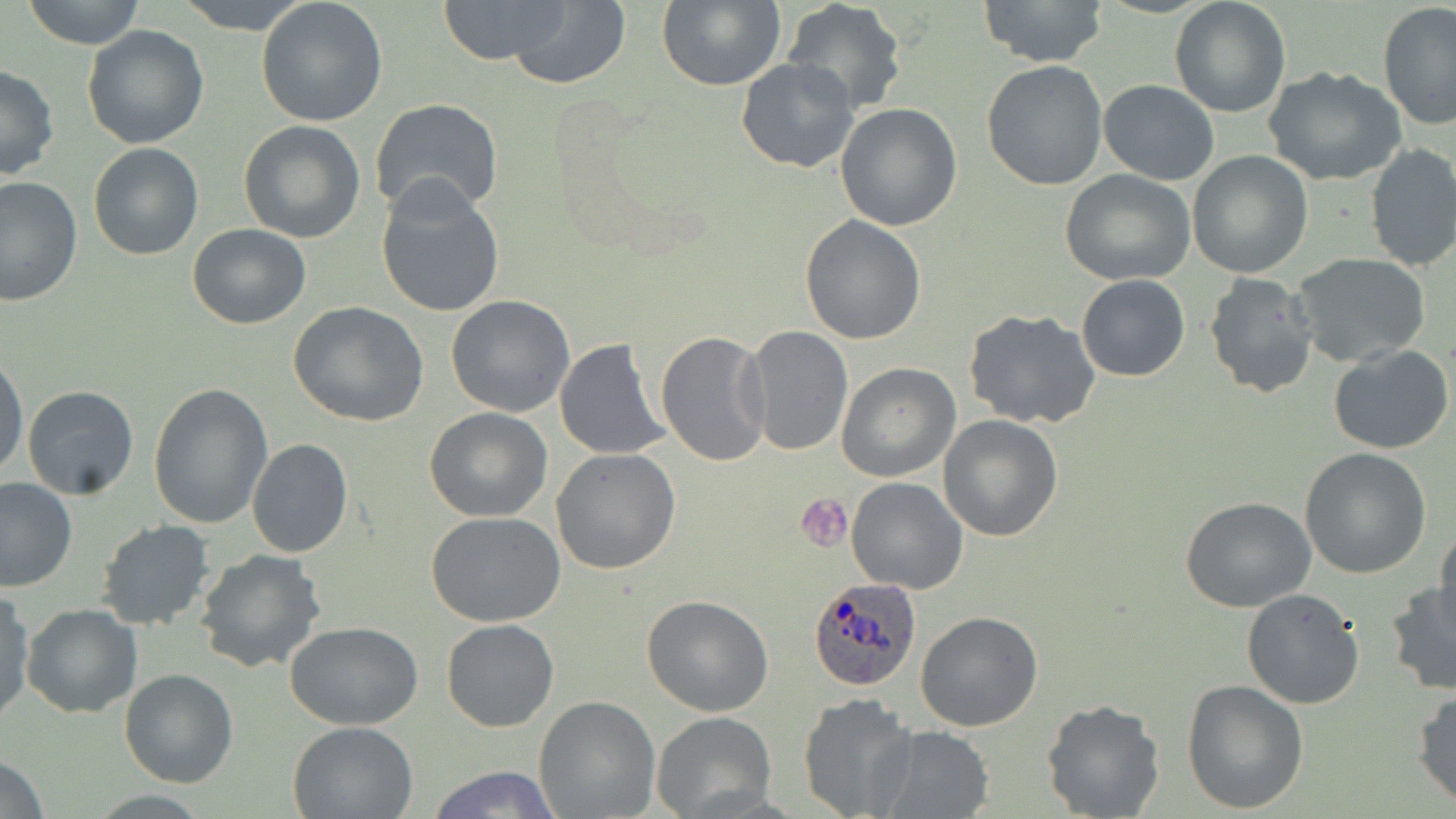 Approximate bounding boxes as (x1, y1, x2, y2) in pixels. Plasmodium ovale-infected red blood cell locations: (808, 578, 921, 691). Platelet locations: (796, 494, 853, 552). Uninfected red blood cell locations: (22, 0, 146, 49), (174, 0, 313, 33), (435, 0, 574, 64), (506, 0, 632, 89), (656, 0, 785, 90), (979, 0, 1107, 68), (255, 1, 388, 126), (1169, 1, 1291, 117), (782, 2, 908, 115), (1377, 4, 1456, 130), (81, 24, 210, 149), (735, 56, 860, 173), (981, 61, 1107, 190), (0, 64, 59, 180), (1265, 67, 1408, 186), (1099, 80, 1219, 184), (370, 99, 504, 221), (834, 103, 963, 231), (238, 120, 366, 242), (88, 141, 203, 260), (1364, 143, 1456, 273), (1187, 151, 1314, 278), (1060, 168, 1197, 285), (1, 176, 81, 306), (376, 178, 506, 319), (799, 215, 927, 344), (186, 221, 312, 330), (1293, 254, 1432, 367), (1203, 272, 1320, 398), (1076, 274, 1190, 383), (445, 294, 576, 417), (288, 302, 430, 426), (962, 308, 1102, 429), (742, 326, 854, 456), (656, 330, 773, 468), (554, 337, 671, 461), (1329, 345, 1453, 455), (0, 350, 28, 483), (836, 362, 960, 481), (148, 382, 274, 528), (22, 383, 139, 499), (425, 406, 552, 523), (938, 414, 1064, 541), (246, 438, 352, 557), (1300, 447, 1433, 578), (550, 449, 680, 575), (845, 476, 967, 593), (0, 477, 76, 592), (1179, 495, 1318, 611), (426, 512, 568, 626), (97, 520, 216, 631), (1433, 528, 1456, 630), (194, 548, 328, 676), (1385, 581, 1456, 695), (0, 588, 34, 723), (1241, 588, 1365, 710), (642, 595, 774, 716), (21, 603, 142, 717), (914, 610, 1043, 732), (442, 618, 559, 731), (285, 621, 424, 730), (118, 668, 237, 788), (1181, 679, 1309, 813), (1412, 689, 1456, 808), (798, 692, 917, 819), (534, 696, 660, 818), (1040, 699, 1165, 819), (652, 711, 776, 819), (288, 719, 419, 818), (873, 727, 995, 818), (0, 754, 49, 818), (425, 764, 562, 819). Slide-level diagnosis: Plasmodium ovale. Captured at 1000x magnification. Single field of view. Light microscopy. Thin blood smear. Image is 1456×819 pixels. May-Grünwald-Giemsa-stained preparation.